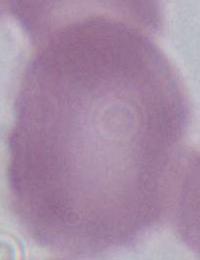
Summary:
  - Magnification: 1000x
  - Identification: red blood cell
  - Modality: micrograph